Name the parasite shown.
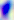
This is Toxoplasma gondii.

modality = photomicrograph
magnification = 400x